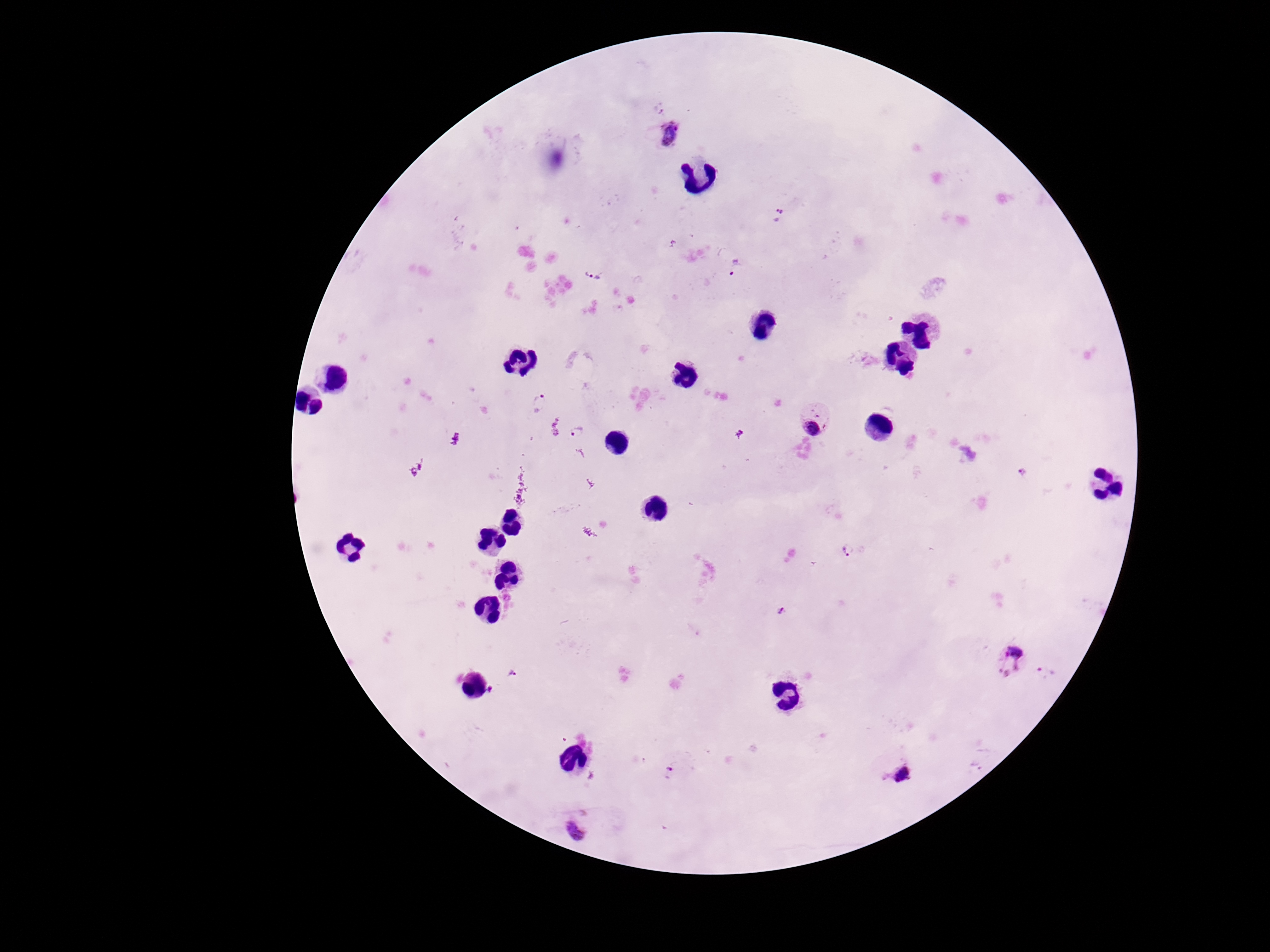

plasmodium_parasite_locations: 'approximate centers as {x, y} in pixels: {661, 105}, {671, 137}, {778, 214}, {734, 267}, {593, 275}, {541, 403}, {815, 420}, {576, 432}, {1022, 473}, {847, 550}, {783, 611}, {1010, 660}, {1046, 673}, {513, 675}, {490, 693}, {668, 770}, {897, 775}, {577, 826}'
field_of_view: one from this slide
stain: Giemsa
patient_malaria_status: positive
image_size: 1270×952 pixels
preparation: thick peripheral-blood smear
capture: smartphone camera through the microscope eyepiece
magnification: 100x